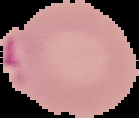
Cell region segmented out of the field of view; the surrounding area is masked to black. Image is 139×118 pixels. From a thin blood film. Malaria status: parasitized.